Locate every malaria parasite and every leukocyte.
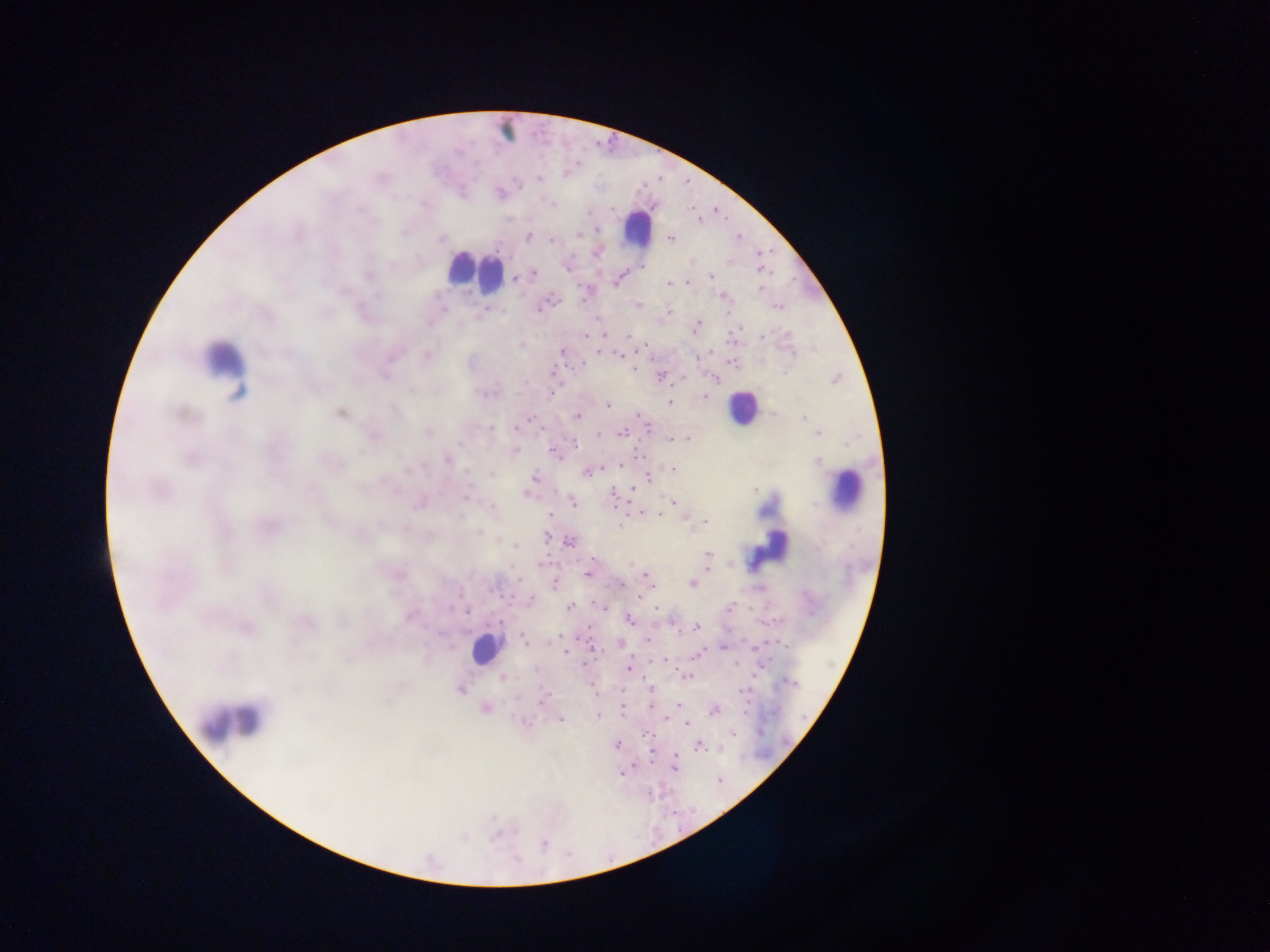

Approximate centers as x y in pixels.
Malaria parasites: 566 174; 538 178; 518 184; 550 203; 611 209; 692 209; 598 230; 578 234; 527 237; 738 237; 671 238; 442 239; 552 240; 596 253; 567 266; 534 273; 368 276; 711 276; 517 278; 616 281; 687 282; 669 284; 760 289; 377 296; 723 297; 639 304; 778 306; 540 308; 443 309; 487 311; 669 312; 483 315; 697 327; 584 335; 630 337; 762 338; 521 345; 562 350; 427 356; 620 356; 698 356; 581 364; 634 369; 552 372; 384 376; 660 376; 716 379; 836 379; 412 389; 551 393; 488 394; 704 397; 669 402; 608 405; 393 410; 772 413; 339 414; 639 415; 578 416; 804 419; 527 421; 489 428; 650 429; 428 432; 623 433; 599 434; 817 434; 672 438; 687 438; 574 443; 515 450; 554 452; 447 460; 818 461; 621 465; 674 469; 587 472; 491 474; 534 477; 649 477; 633 489; 755 490; 527 494; 466 496; 613 496; 674 502; 573 503; 641 513; 551 514; 659 514; 705 521; 620 525; 478 533; 546 536; 569 542; 708 555; 707 560; 631 564; 588 573; 649 578; 620 584; 691 584; 554 585; 531 600; 599 605; 569 607; 603 607; 730 608; 465 610; 410 616; 629 619; 672 621; 500 622; 697 627; 523 638; 648 639; 621 644; 723 648; 565 652; 698 654; 664 660; 735 664; 629 668; 686 677; 502 678; 788 682; 460 690; 651 690; 741 691; 542 700; 679 704; 484 708; 622 709; 713 710; 598 715; 561 720; 687 723; 645 732; 734 733; 616 745; 698 747; 674 767; 719 779; 544 844.
Leukocytes: 504 131; 638 230; 466 270; 489 274; 223 360; 742 407; 847 490; 768 540; 485 649; 235 720.

{
  "image_size": "1270×952 pixels",
  "preparation": "thick blood smear",
  "country": "Ghana",
  "field_of_view": "single",
  "capture": "mobile-phone photograph through a microscope"
}